Locate and identify every blood parasite.
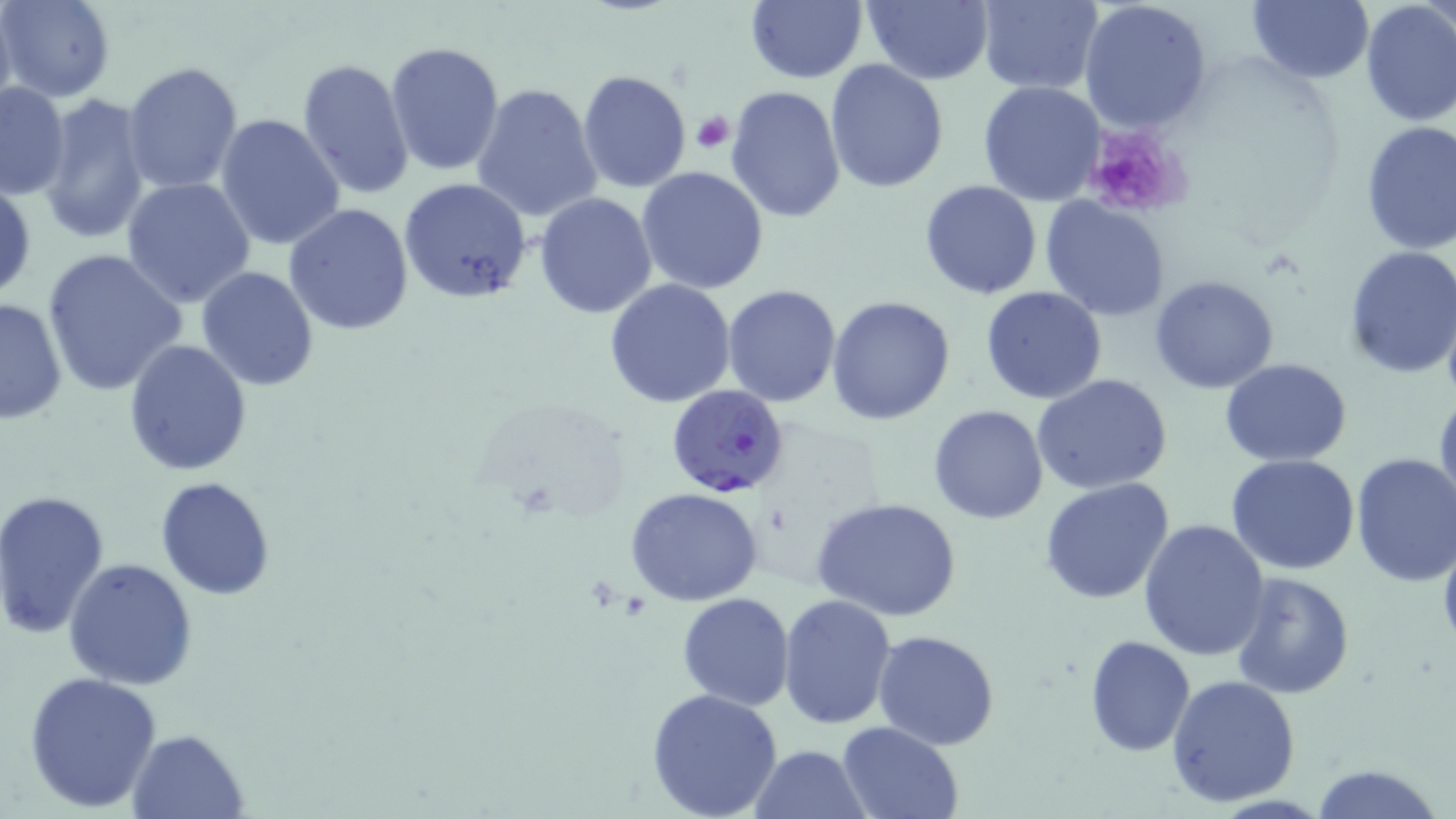

Approximate bounding boxes as (x1,y1)-(x2,y2) corner pairs in pixels.
Plasmodium falciparum-infected red blood cells: (668,384)-(788,498).
No Plasmodium ovale, Plasmodium malariae, Plasmodium vivax, Babesia divergens, or Trypanosoma brucei observed.

Uninfected red blood cell locations: (2,0)-(115,102), (745,0)-(867,83), (861,0)-(994,85), (975,0)-(1102,92), (1079,0)-(1212,133), (1245,0)-(1374,86), (1358,3)-(1456,130), (385,40)-(505,176), (297,57)-(414,198), (824,59)-(949,194), (122,60)-(243,196), (575,68)-(691,193), (978,80)-(1107,206), (0,82)-(71,199), (470,82)-(604,223), (725,86)-(847,224), (37,92)-(151,243), (215,114)-(346,251), (1358,121)-(1456,254), (636,166)-(770,295), (122,177)-(256,307), (398,177)-(531,304), (0,178)-(36,304), (919,181)-(1042,299), (534,192)-(657,319), (1040,197)-(1170,321), (284,203)-(415,336), (1342,245)-(1456,379), (41,247)-(186,397), (196,265)-(321,392), (1150,275)-(1278,393), (604,278)-(735,407), (721,284)-(843,407), (980,286)-(1106,404), (1,296)-(66,427), (827,296)-(956,426), (123,339)-(253,475), (1220,358)-(1352,467), (1033,373)-(1174,496), (1433,385)-(1456,524), (928,404)-(1049,524), (1350,452)-(1456,588), (1227,453)-(1362,574), (154,476)-(276,599), (1040,478)-(1175,606), (626,489)-(765,606), (1,490)-(112,639), (813,496)-(962,623), (1137,518)-(1270,662), (63,557)-(197,689), (1231,570)-(1357,699), (678,592)-(795,710), (777,592)-(898,730), (873,629)-(999,749), (1084,635)-(1194,755), (22,670)-(165,812), (1166,674)-(1301,808), (646,688)-(782,817), (835,721)-(964,818), (126,728)-(251,818), (750,743)-(870,818), (1307,763)-(1445,819). Platelet locations: (691,111)-(734,154), (1079,124)-(1189,219). Slide-level diagnosis: Plasmodium falciparum. One field of a larger specimen. May-Grünwald-Giemsa stain. Light microscopy. 1000x magnification. Image is 1456×819 pixels. Thin blood smear.